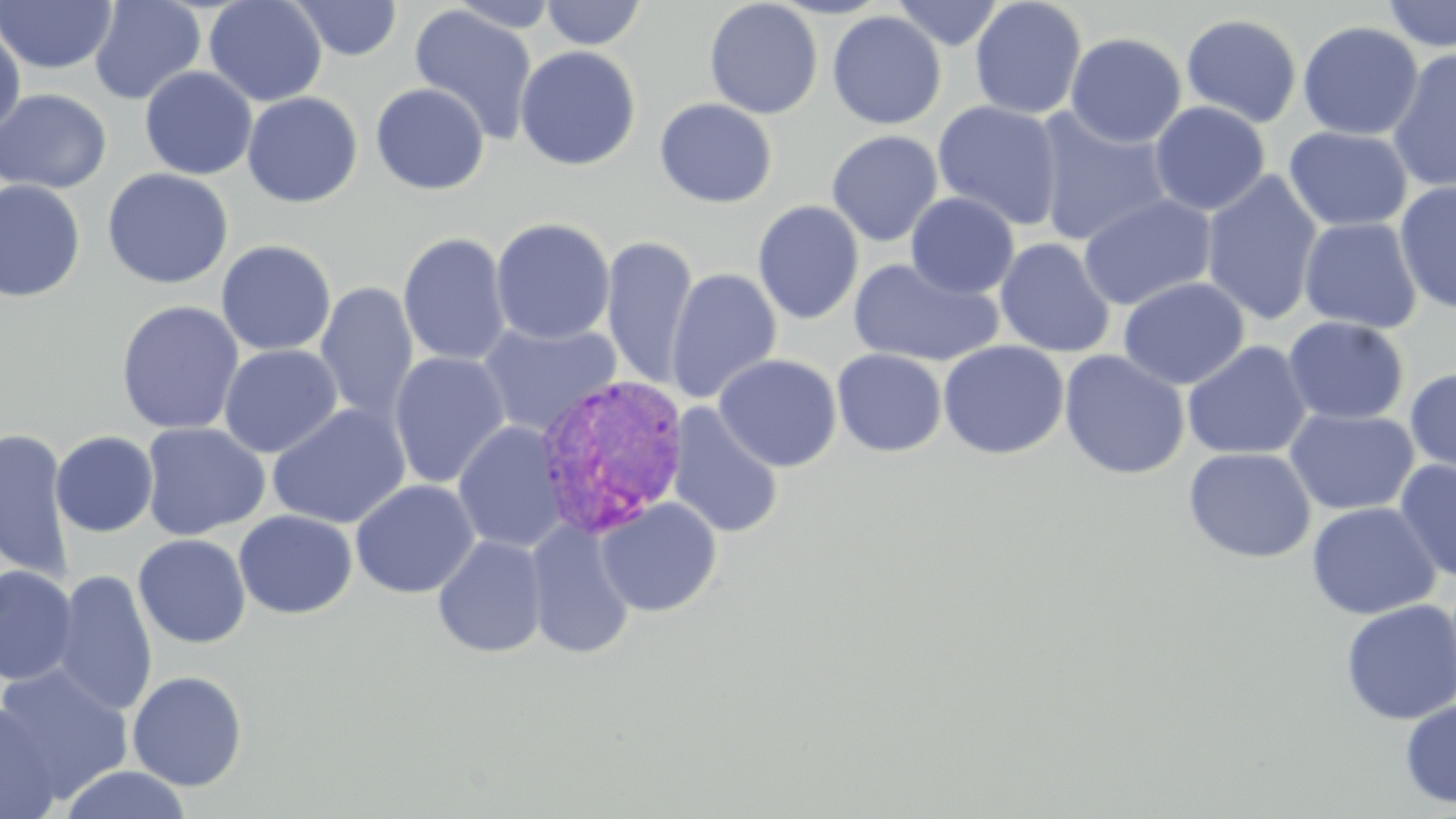
Plasmodium vivax-infected red blood cell locations = approximate bounding boxes as [x1, y1, x2, y2] in pixels: [532, 373, 693, 539]
slide-level diagnosis = Plasmodium vivax
stain = May-Grünwald-Giemsa
image size = 1456×819 pixels
preparation = thin blood smear
magnification = 1000x
modality = optical microscopy
uninfected red blood cell locations = approximate bounding boxes as [x1, y1, x2, y2] in pixels: [89, 0, 206, 105], [203, 0, 328, 107], [289, 0, 403, 61], [704, 0, 823, 119], [767, 0, 893, 19], [891, 0, 1005, 51], [969, 0, 1087, 120], [1382, 0, 1456, 52], [0, 1, 118, 74], [442, 1, 566, 34], [540, 1, 647, 49], [408, 4, 539, 145], [827, 10, 947, 130], [1180, 13, 1303, 128], [0, 21, 26, 139], [1297, 21, 1423, 140], [1065, 32, 1187, 148], [514, 45, 642, 171], [1387, 48, 1456, 193], [139, 67, 258, 180], [370, 83, 490, 195], [0, 88, 112, 194], [242, 92, 363, 207], [654, 98, 778, 208], [933, 100, 1064, 231], [1148, 101, 1271, 216], [1033, 108, 1175, 248], [1283, 126, 1412, 232], [826, 130, 944, 247], [102, 168, 233, 290], [1200, 170, 1323, 327], [0, 180, 87, 302], [1395, 181, 1456, 315], [906, 192, 1020, 298], [1078, 194, 1217, 310], [752, 200, 865, 325], [491, 217, 615, 344], [1299, 217, 1423, 334], [397, 232, 511, 366], [601, 236, 699, 390], [995, 237, 1116, 359], [216, 240, 336, 356], [847, 257, 1004, 368], [665, 267, 782, 405], [1118, 276, 1249, 390], [315, 282, 419, 424], [116, 300, 245, 435], [1283, 316, 1409, 425], [476, 320, 621, 438], [937, 340, 1070, 460], [1181, 340, 1312, 460], [219, 345, 342, 458], [832, 349, 947, 457], [1059, 349, 1191, 480], [389, 352, 510, 489], [713, 353, 843, 472], [1404, 367, 1456, 477], [267, 404, 410, 528], [667, 404, 784, 540], [1284, 407, 1419, 515], [453, 421, 568, 554], [140, 422, 270, 541], [0, 427, 75, 584], [50, 431, 159, 538], [1183, 446, 1316, 564], [1394, 459, 1456, 584], [350, 479, 480, 598], [595, 497, 722, 617], [1306, 501, 1441, 620], [234, 510, 358, 619], [525, 518, 637, 660], [133, 534, 251, 649], [431, 535, 548, 659], [1, 565, 79, 686], [51, 570, 158, 716], [1340, 599, 1456, 725], [0, 663, 133, 803], [127, 671, 248, 791], [1399, 698, 1456, 809], [0, 704, 61, 819], [59, 765, 194, 819]
field of view = one of a larger specimen